State which parasite is depicted.
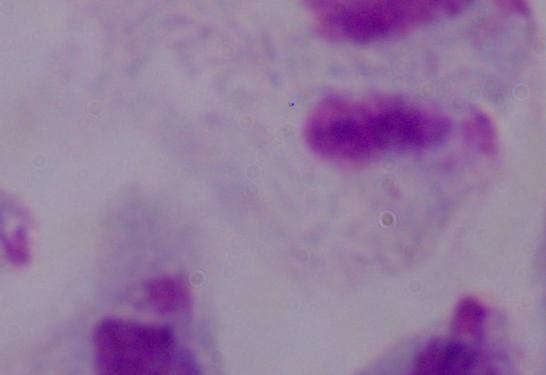

A trichomonad.

Photomicrograph. Captured at 1000x magnification.